Give the preparation type.
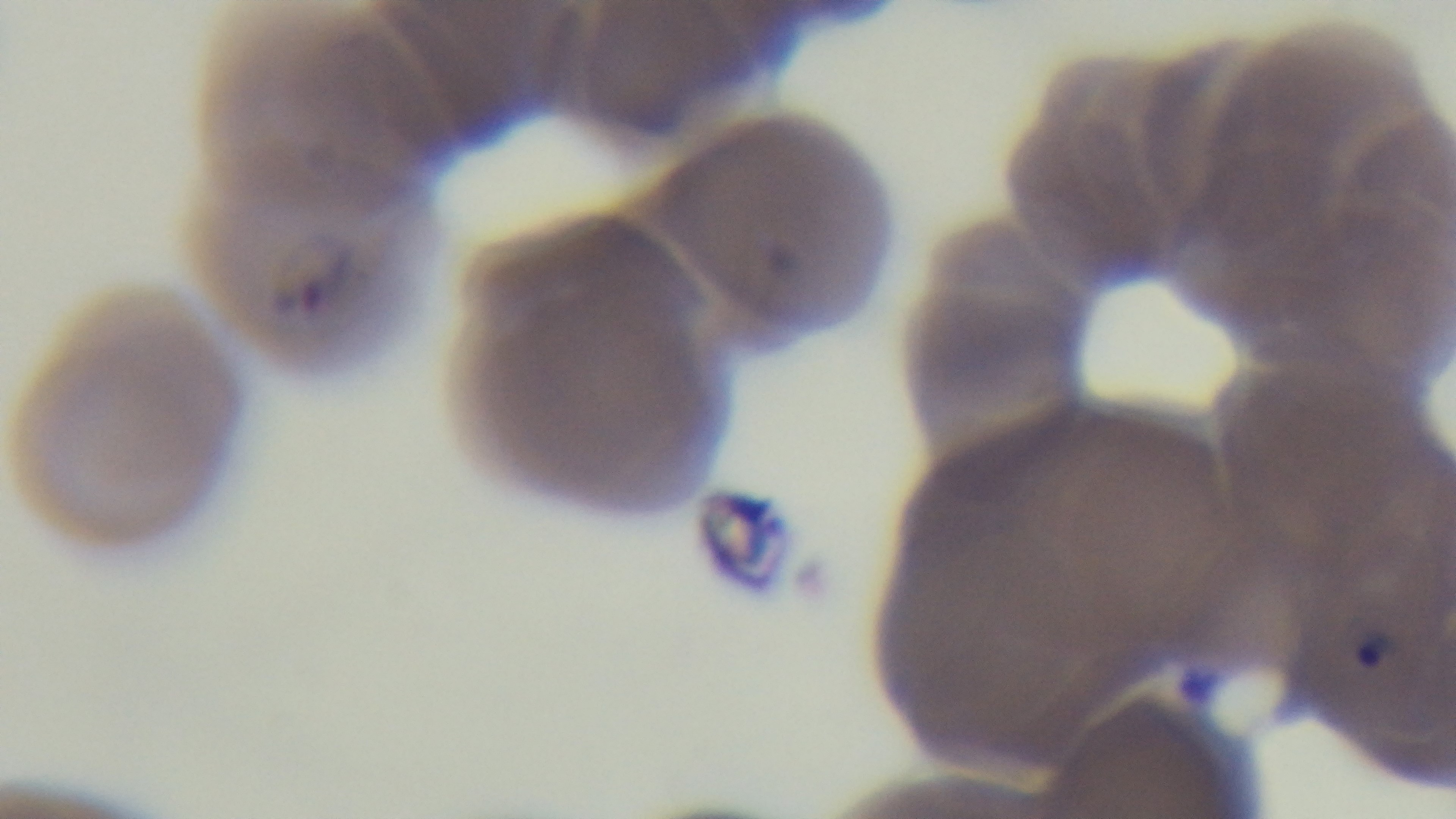

Thin.

Summary:
  - Modality: light microscopy
  - Objective: 100x oil immersion
  - Capture: mounted 4K digital camera
  - Malaria status: positive
  - Stain: Giemsa
  - Field of view: single